Name the blood parasite species.
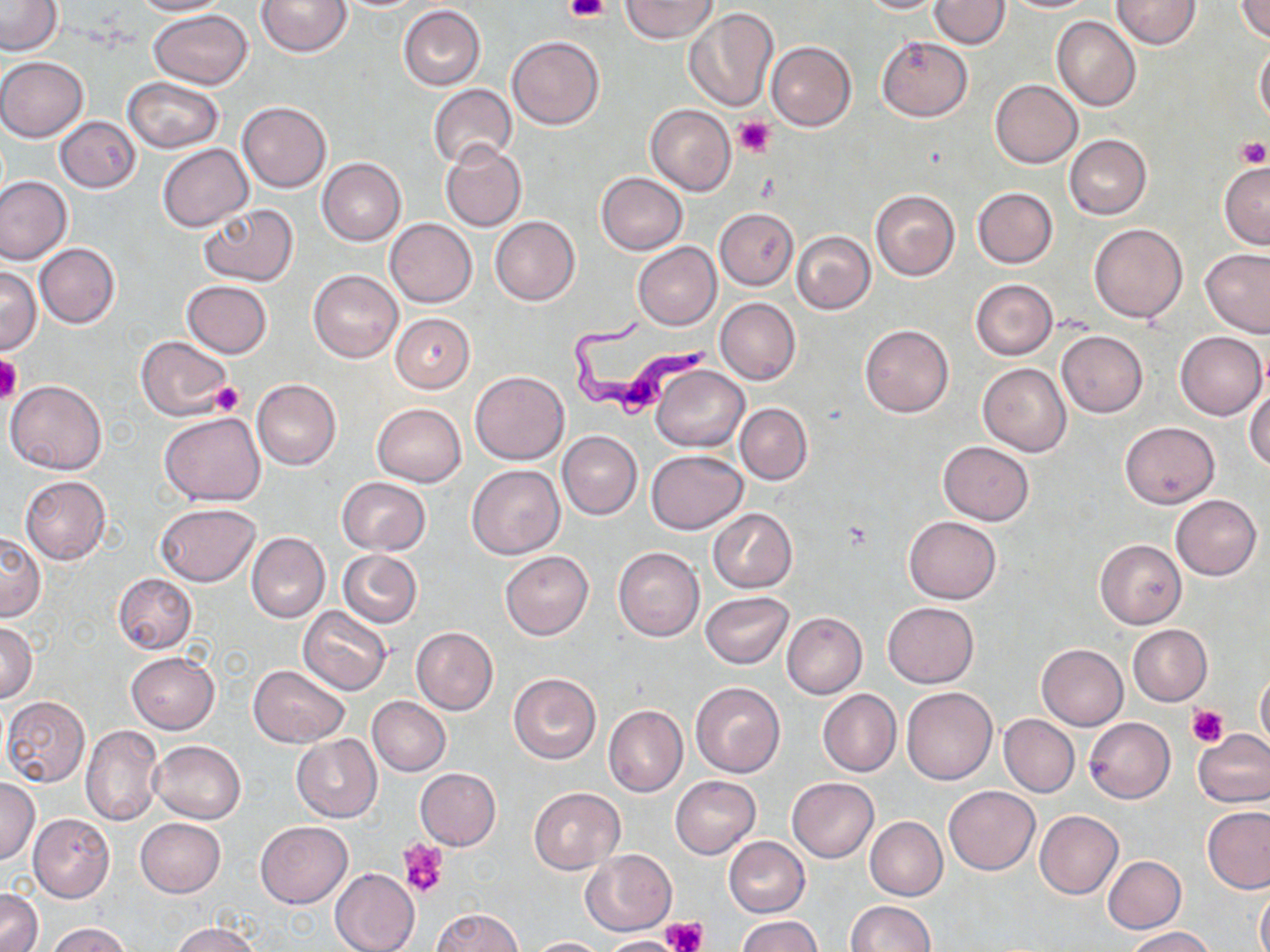

Trypanosoma brucei.

Approximate bounding boxes as (x1,y1)-(x2,y2) corner pairs in pixels. Trypanosoma brucei locations: (566,313)-(715,419). Uninfected red blood cell locations: (131,0)-(229,16), (258,0)-(351,57), (621,0)-(718,42), (855,0)-(945,13), (930,0)-(1011,49), (1005,0)-(1097,13), (1111,0)-(1202,50), (1234,0)-(1270,42), (0,1)-(62,56), (399,4)-(485,90), (682,7)-(781,112), (148,10)-(253,89), (1051,15)-(1140,111), (507,35)-(604,130), (876,35)-(973,121), (766,41)-(857,130), (1255,42)-(1270,124), (0,56)-(88,142), (122,77)-(223,152), (991,79)-(1082,169), (428,84)-(517,168), (237,102)-(331,192), (646,105)-(736,195), (55,116)-(141,193), (1064,135)-(1151,219), (440,143)-(526,232), (156,144)-(253,232), (317,158)-(406,245), (1218,159)-(1270,249), (596,172)-(688,254), (0,176)-(72,265), (972,187)-(1058,268), (870,189)-(960,281), (199,204)-(299,286), (715,208)-(799,290), (489,215)-(580,306), (385,218)-(477,308), (1089,223)-(1187,323), (791,231)-(875,314), (632,242)-(721,330), (35,244)-(120,327), (1199,248)-(1270,337), (1,266)-(41,353), (308,270)-(402,362), (971,279)-(1058,361), (182,280)-(272,359), (716,298)-(800,385), (390,313)-(475,392), (860,324)-(954,417), (1056,330)-(1147,418), (1175,331)-(1267,421), (135,337)-(232,420), (978,363)-(1072,456), (653,365)-(749,452), (471,370)-(569,465), (6,378)-(106,475), (252,378)-(340,469), (1246,386)-(1270,471), (371,403)-(466,487), (735,404)-(811,484), (160,412)-(265,506), (1121,422)-(1219,508), (557,431)-(641,519), (938,440)-(1035,525), (647,450)-(746,533), (468,465)-(565,559), (20,476)-(110,564), (337,477)-(431,555), (1170,495)-(1261,579), (155,503)-(260,586), (709,509)-(796,593), (903,516)-(1001,603), (246,531)-(329,623), (0,532)-(44,621), (1095,539)-(1186,628), (613,547)-(704,641), (338,549)-(422,628), (500,550)-(594,640), (114,574)-(196,654), (700,591)-(795,669), (883,602)-(978,687), (298,606)-(392,695), (782,612)-(867,699), (0,621)-(38,703), (1128,624)-(1211,705), (411,627)-(498,716), (1037,644)-(1127,730), (125,652)-(220,734), (248,664)-(349,746), (1256,669)-(1270,755), (508,673)-(602,764), (690,681)-(786,778), (901,686)-(997,785), (818,689)-(900,777), (1,695)-(91,788), (368,696)-(450,775), (604,705)-(687,795), (998,714)-(1080,796), (1084,718)-(1175,802), (80,724)-(164,827), (1194,727)-(1270,807), (292,734)-(381,821), (151,740)-(245,823), (415,767)-(501,850), (670,775)-(762,859), (0,778)-(39,864), (787,778)-(879,862), (943,785)-(1039,875), (528,787)-(624,873), (1201,805)-(1270,893), (1035,810)-(1123,898), (28,814)-(114,903), (864,816)-(947,899), (135,818)-(225,896), (255,821)-(352,908), (723,837)-(809,917), (580,849)-(676,936), (1103,855)-(1186,933), (330,867)-(419,952), (1255,881)-(1270,952), (1,888)-(42,952), (846,900)-(933,951), (431,908)-(524,952), (736,915)-(822,952), (46,922)-(132,952), (172,922)-(262,952), (1124,927)-(1216,951), (600,935)-(687,952), (528,936)-(609,951). Platelet locations: (564,0)-(611,24), (734,117)-(776,158), (1234,137)-(1270,168), (0,357)-(22,405), (210,381)-(245,416), (1188,705)-(1227,748), (401,840)-(448,898), (665,917)-(706,952). Thin blood film. Image is 1270×952 pixels. Light microscopy. May-Grünwald-Giemsa-stained preparation. Captured at 1000x magnification. One field of a larger specimen.